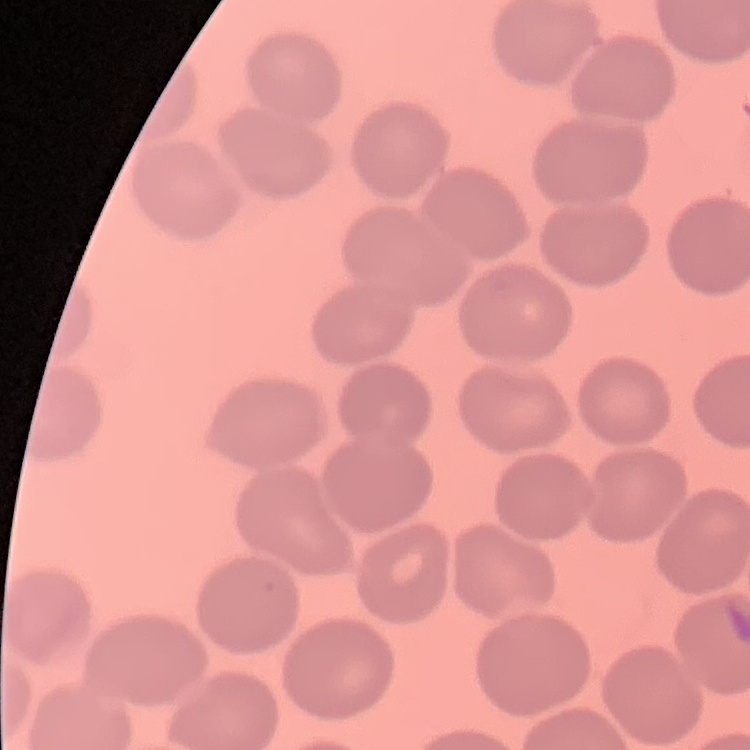 The erythrocytes exhibit no rouleaux formation. Thin peripheral smear. One tile cut from a larger photomicrograph. Stained with either Field's or Giemsa.